Classify this cell by malaria status.
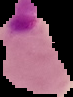

Parasitized.

preparation = thin blood smear
image size = 73×97 pixels
image type = cell region segmented out of the field of view; surrounding area masked to black